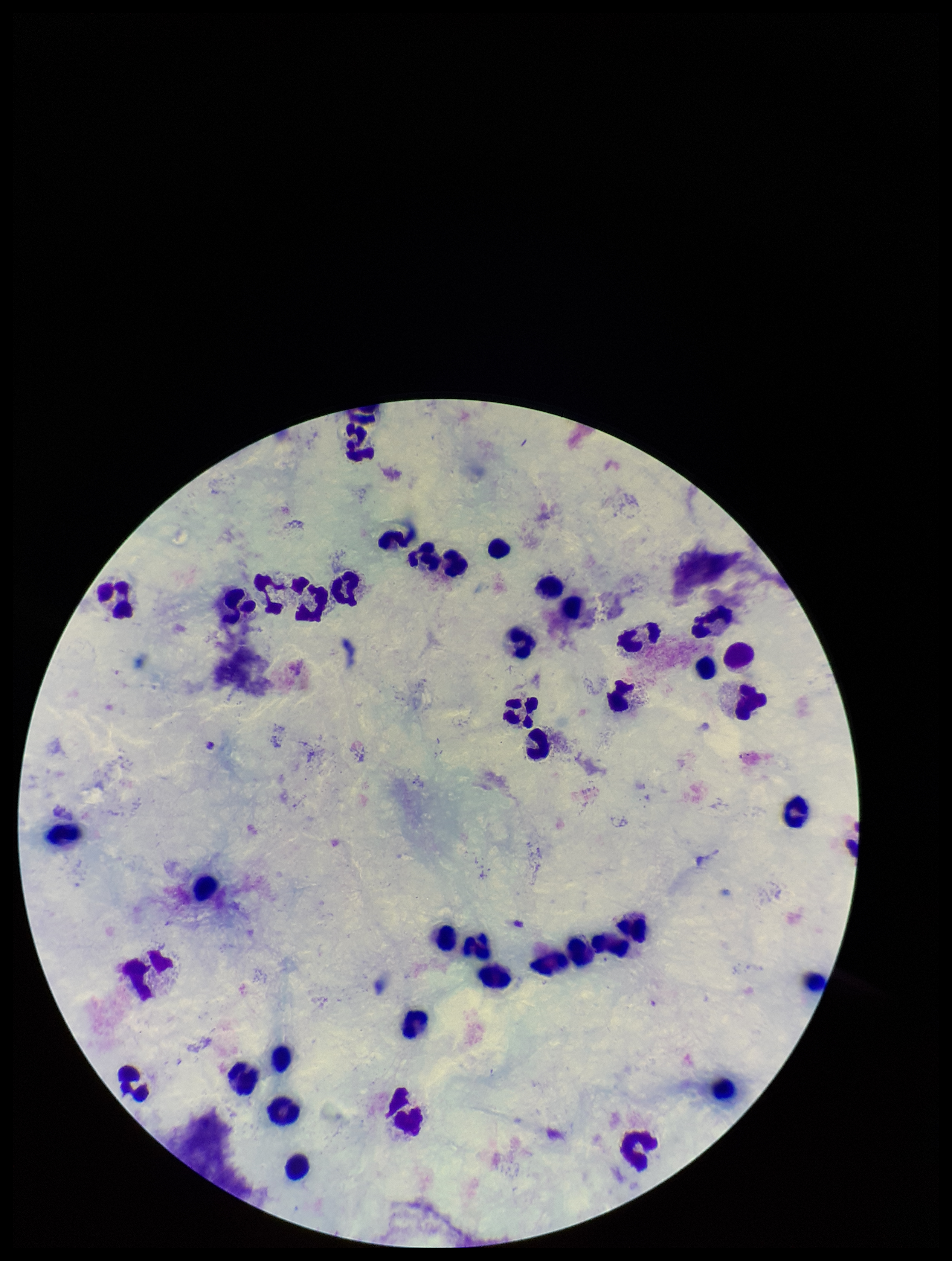
Summary:
  - Parasite count: 0
  - Stain: Giemsa
  - Field of view: single
  - Plasmodium parasites: none detected
  - Patient malaria status: negative
  - Capture: smartphone photograph through the microscope eyepiece
  - Leukocyte count: 45
  - Image size: 952×1261 pixels
  - Preparation: thick smear